Evaluate for Plasmodium parasites.
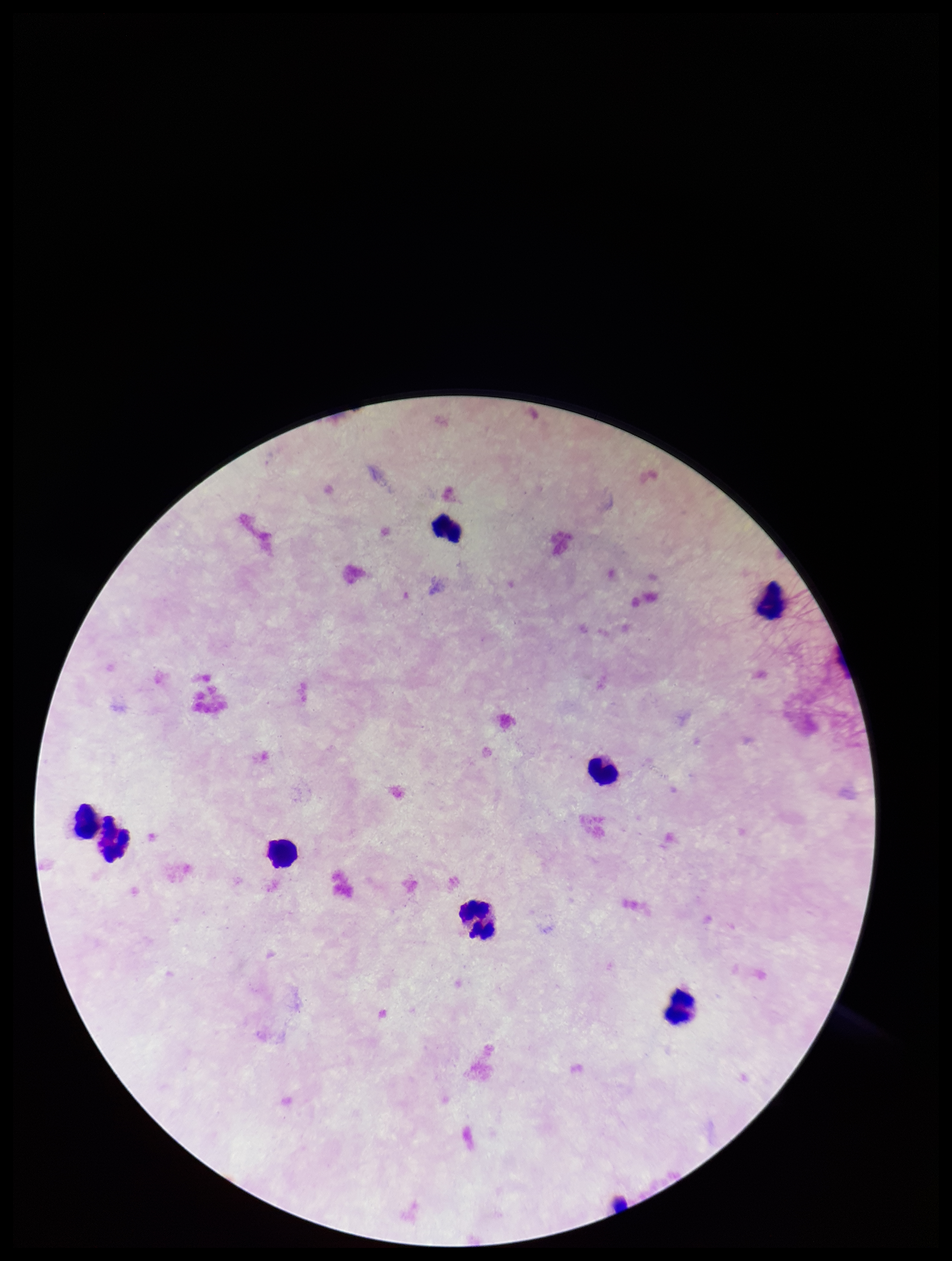
None identified.

Summary:
  - Field of view: single
  - Leukocyte count: 8
  - Patient malaria status: negative
  - Image size: 952×1261 pixels
  - Capture: smartphone photograph through the microscope eyepiece
  - Stain: Giemsa
  - Parasite count: 0
  - Preparation: thick